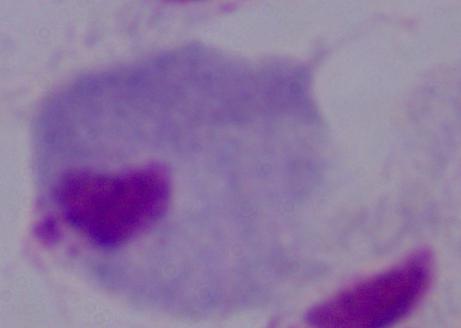
{
  "identification": "trichomonad",
  "magnification": "1000x",
  "modality": "photomicrograph"
}